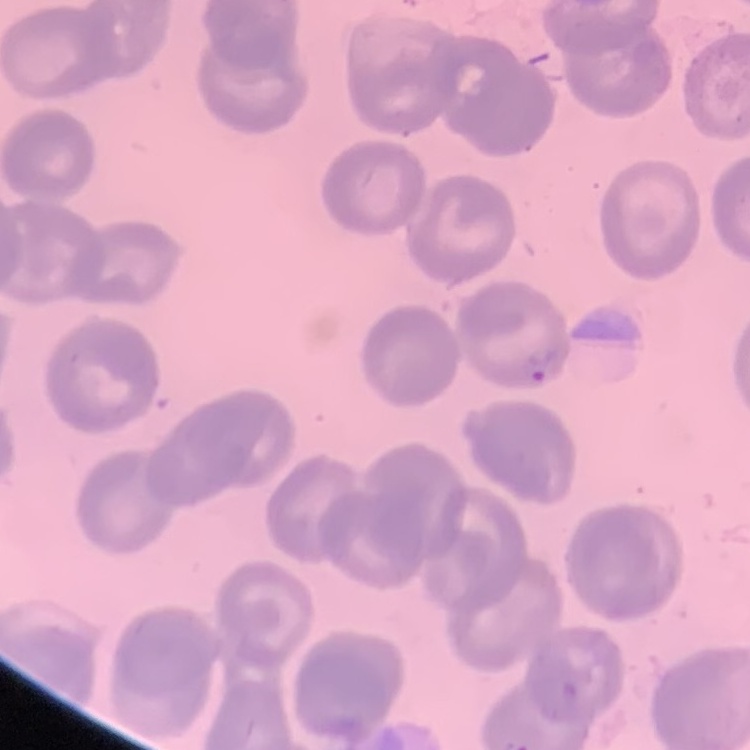

The erythrocytes exhibit no rouleaux formation. Field's or Giemsa stain. Thin blood film. One tile cut from a larger photomicrograph.